Assess the morphology of the red blood cells.
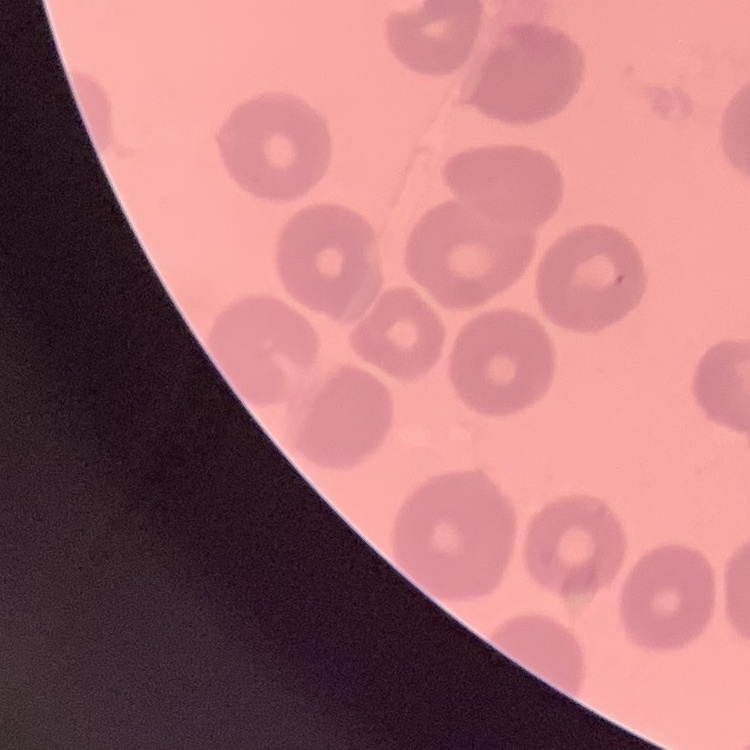

No rouleaux formation.

image type = one tile cut from a larger photomicrograph
stain = Field's or Giemsa
preparation = thin peripheral smear